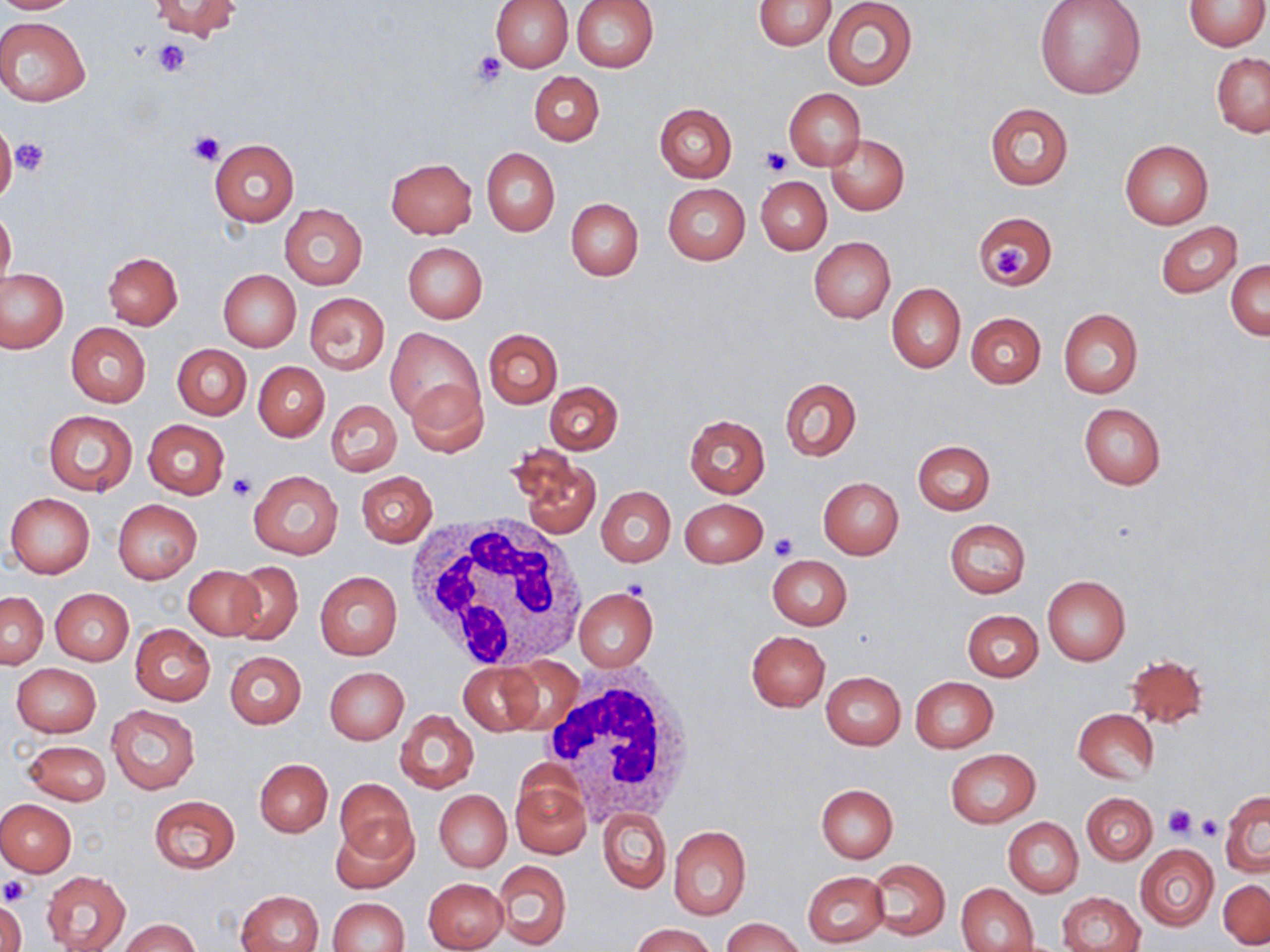

Summary:
  - Coordinate format: approximate bounding boxes as [x1, y1, x2, y2] in pixels
  - Uninfected red blood cell locations: [0, 0, 82, 13], [149, 0, 242, 42], [489, 0, 573, 72], [571, 0, 659, 72], [753, 0, 837, 50], [1034, 0, 1147, 102], [1184, 0, 1268, 50], [822, 1, 916, 90], [0, 17, 91, 106], [1211, 53, 1270, 136], [530, 71, 604, 145], [783, 88, 867, 170], [984, 102, 1074, 191], [656, 104, 736, 182], [0, 126, 17, 205], [827, 135, 909, 215], [209, 139, 299, 226], [1119, 140, 1214, 229], [482, 147, 559, 236], [385, 157, 477, 238], [754, 175, 831, 254], [662, 183, 750, 264], [566, 198, 642, 281], [279, 203, 368, 289], [0, 206, 16, 294], [973, 211, 1057, 291], [1156, 221, 1242, 298], [808, 236, 896, 323], [402, 242, 488, 323], [102, 251, 183, 328], [1227, 260, 1269, 340], [1, 267, 68, 353], [217, 269, 301, 351], [886, 283, 965, 373], [305, 293, 389, 374], [1058, 308, 1142, 399], [966, 312, 1045, 387], [66, 323, 151, 407], [385, 328, 483, 426], [484, 329, 562, 408], [172, 344, 251, 418], [254, 362, 328, 441], [405, 378, 488, 456], [781, 378, 861, 460], [545, 381, 623, 454], [326, 399, 402, 478], [1079, 403, 1166, 489], [44, 410, 138, 497], [685, 415, 769, 497], [144, 420, 230, 499], [913, 440, 994, 514], [515, 452, 600, 536], [248, 469, 343, 560], [356, 472, 437, 546], [818, 477, 904, 559], [596, 486, 675, 567], [6, 492, 95, 578], [680, 497, 769, 569], [113, 500, 202, 583], [944, 518, 1030, 598], [767, 555, 851, 630], [226, 561, 303, 644], [185, 566, 265, 640], [315, 572, 403, 660], [1041, 576, 1129, 666], [50, 588, 134, 665], [573, 588, 657, 671], [1, 590, 47, 668], [963, 610, 1043, 681], [129, 624, 215, 705], [746, 631, 830, 711], [225, 651, 306, 728], [1123, 653, 1209, 728], [498, 659, 584, 736], [456, 663, 543, 735], [12, 664, 101, 738], [324, 666, 409, 744], [821, 671, 906, 750], [910, 676, 998, 753], [107, 705, 200, 793], [1073, 708, 1158, 783], [394, 710, 479, 794], [23, 741, 110, 804], [945, 749, 1038, 827], [255, 758, 332, 836], [511, 769, 590, 859], [333, 778, 416, 864], [816, 784, 898, 863], [435, 790, 510, 871], [1220, 791, 1270, 876], [1082, 792, 1156, 863], [149, 795, 239, 873], [0, 799, 76, 876], [599, 807, 671, 894], [330, 813, 419, 894], [1003, 817, 1083, 897], [669, 827, 751, 921], [1136, 844, 1218, 929], [494, 860, 572, 949], [869, 860, 949, 939], [42, 870, 131, 952], [804, 872, 888, 947], [423, 877, 508, 952], [1220, 879, 1269, 948], [956, 883, 1038, 952], [236, 890, 325, 952], [1057, 891, 1144, 952], [328, 897, 409, 951], [1, 899, 25, 952], [120, 918, 198, 952], [724, 918, 803, 952], [630, 922, 714, 952]
  - White blood cell locations: [407, 513, 590, 672], [537, 670, 698, 824]
  - Platelet locations: [151, 40, 191, 77], [471, 50, 507, 86], [3, 130, 38, 187], [187, 130, 223, 166], [10, 137, 49, 175], [760, 145, 792, 175], [991, 242, 1029, 283], [226, 471, 256, 502], [768, 533, 798, 561], [1164, 804, 1195, 839], [1197, 816, 1223, 841], [0, 875, 32, 906], [1, 891, 27, 946]
  - Slide-level diagnosis: negative for blood parasites
  - Stain: May-Grünwald-Giemsa
  - Magnification: 1000x
  - Preparation: thin blood smear
  - Modality: light microscopy
  - Image size: 1270×952 pixels
  - Field of view: one of a larger specimen